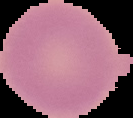

Summary:
  - Result: no Plasmodium parasites detected
  - Image type: cell region segmented out of the field of view; surrounding area masked to black
  - Preparation: thin blood film
  - Image size: 133×118 pixels